Identify the parasite.
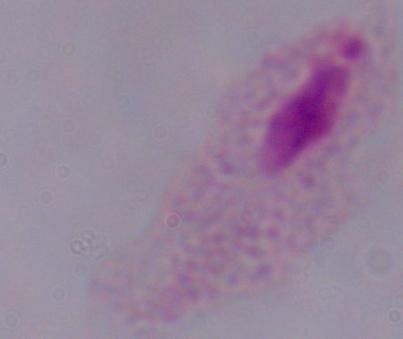
This is a trichomonad.

modality = micrograph
magnification = 1000x